Look for Plasmodium parasites.
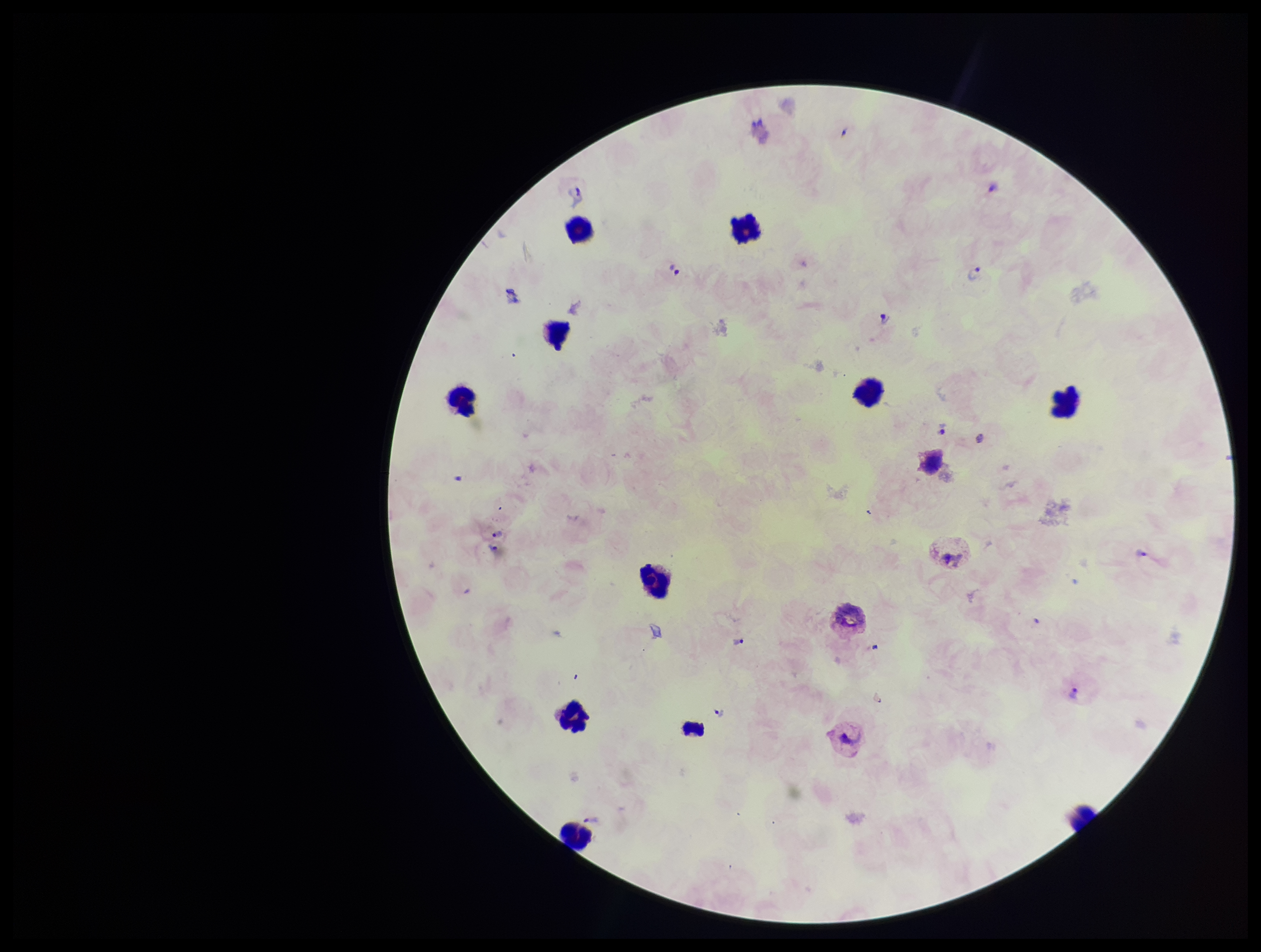
Seen.

parasite count = 13
species reported for this patient = Plasmodium vivax
stain = Giemsa
image size = 1261×952 pixels
leukocyte count = 11
capture = smartphone photograph through the microscope eyepiece
field of view = single
preparation = thick
patient malaria status = infected